Classify this cell by malaria status.
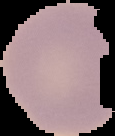

Uninfected.

Cell region segmented out of the field of view; the surrounding area is masked to black. Image is 115×136 pixels. From a thin blood film.